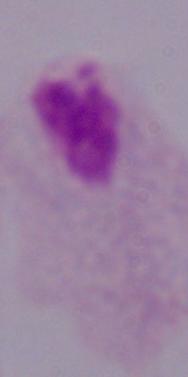
1000x magnification. Photomicrograph. A trichomonad is seen.